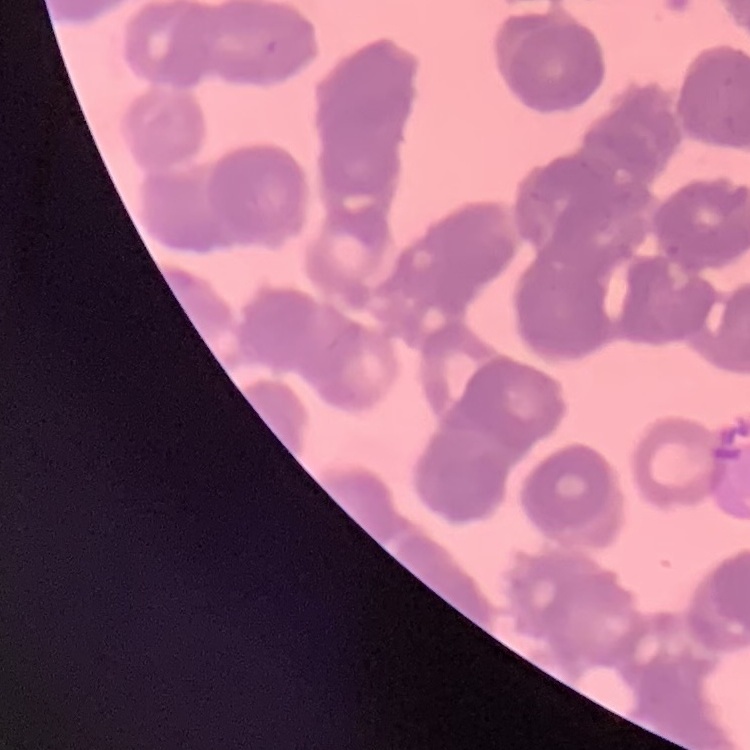
erythrocyte morphology = rouleaux formation
image type = one tile cut from a larger photomicrograph
preparation = thin blood film
stain = Field's or Giemsa